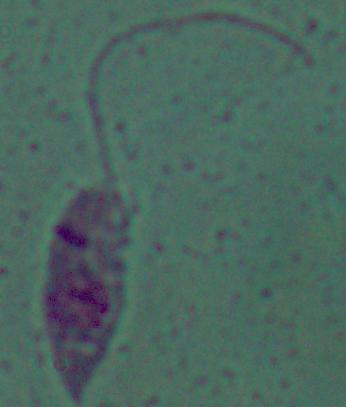

Summary:
  - Magnification: 1000x
  - Identification: Leishmania
  - Modality: micrograph